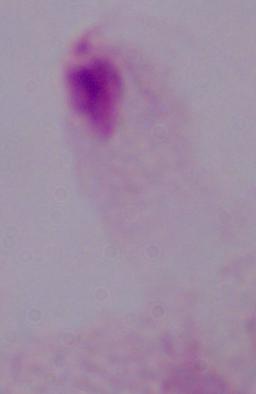

modality = photomicrograph
identification = trichomonad
magnification = 1000x